Locate every blood parasite and identify its species.
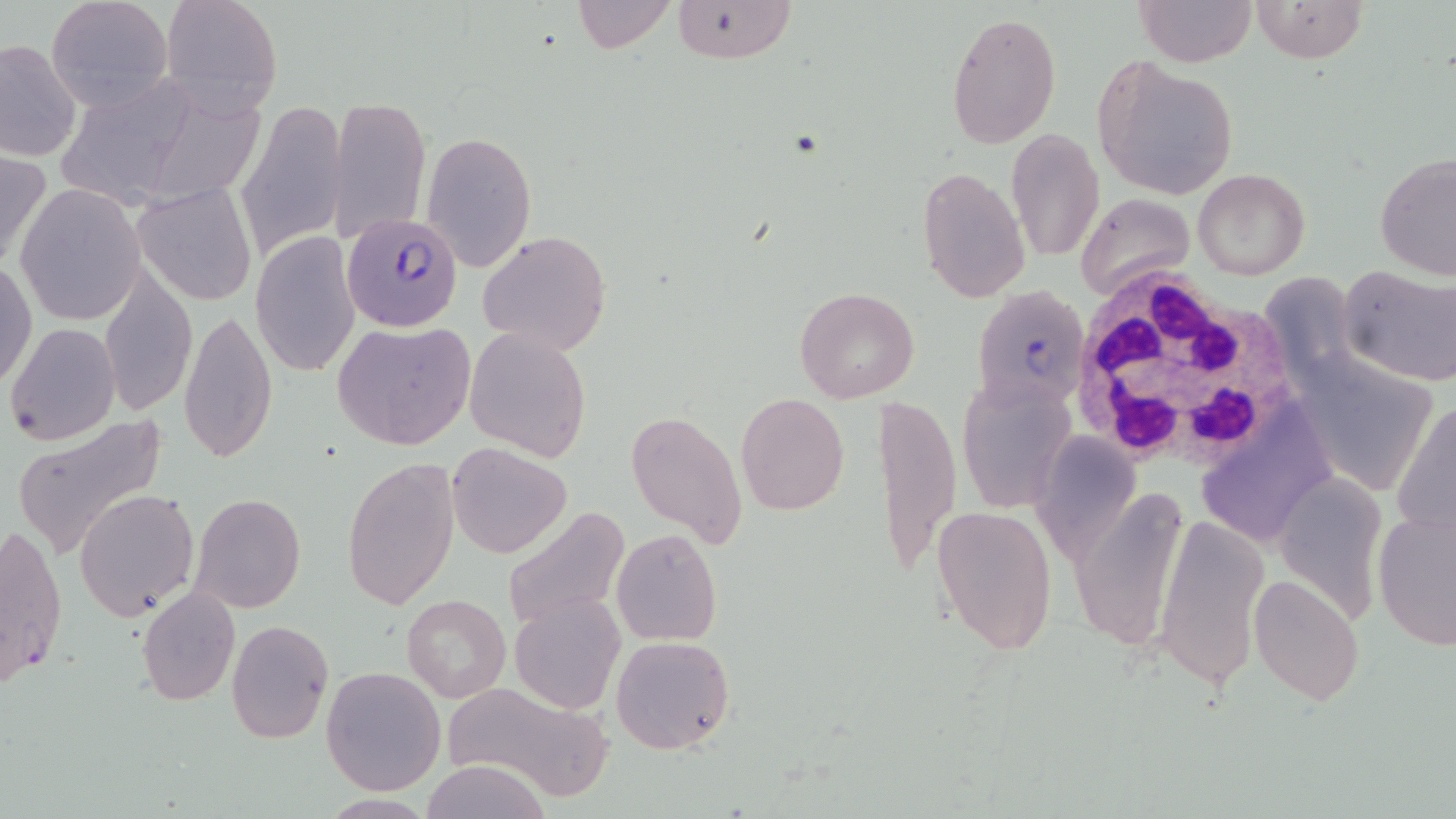

Approximate bounding boxes as (x1,y1)-(x2,y2) corner pairs in pixels.
Plasmodium falciparum-infected red blood cells: (341,210)-(465,333), (972,285)-(1090,415).
No Plasmodium ovale, Plasmodium malariae, Plasmodium vivax, Babesia divergens, or Trypanosoma brucei observed.

Uninfected red blood cell locations: (47,0)-(170,110), (160,0)-(283,117), (570,0)-(676,52), (668,0)-(798,64), (1134,0)-(1257,67), (1250,0)-(1367,64), (947,11)-(1061,149), (1,37)-(82,162), (1092,55)-(1241,202), (47,70)-(220,206), (328,94)-(431,241), (234,99)-(348,261), (1006,130)-(1104,262), (422,131)-(537,272), (0,147)-(49,275), (1373,153)-(1455,283), (916,165)-(1030,301), (1192,168)-(1311,278), (14,183)-(147,325), (131,183)-(257,304), (1074,193)-(1194,300), (479,230)-(610,356), (251,232)-(359,379), (1,260)-(37,391), (1337,264)-(1456,386), (99,267)-(196,417), (1280,284)-(1374,410), (794,286)-(919,404), (179,308)-(278,464), (332,320)-(476,451), (5,323)-(120,445), (464,327)-(592,462), (1310,364)-(1432,492), (957,374)-(1075,515), (736,393)-(849,515), (877,395)-(961,583), (1393,400)-(1456,540), (625,410)-(748,547), (10,414)-(168,559), (1203,414)-(1334,555), (1033,432)-(1140,560), (447,442)-(571,558), (342,456)-(462,612), (1275,472)-(1388,623), (1069,484)-(1193,654), (75,488)-(201,621), (190,491)-(307,613), (932,506)-(1056,657), (501,507)-(631,634), (1373,508)-(1456,650), (1153,514)-(1271,691), (1,523)-(67,688), (611,529)-(722,646), (1249,574)-(1366,706), (136,586)-(240,704), (401,594)-(511,703), (511,594)-(624,714), (226,619)-(332,742), (612,635)-(735,755), (321,665)-(448,796), (437,681)-(613,799), (421,759)-(552,819). White blood cell locations: (1066,266)-(1299,470). Slide-level diagnosis: Plasmodium falciparum. Captured at 1000x magnification. May-Grünwald-Giemsa stain. Single field of view. Image is 1456×819 pixels. Light microscopy. Thin blood film.